Assess this cell for malaria.
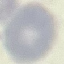

Uninfected.

Summary:
  - Preparation: thin smear
  - Capture: smartphone through the microscope eyepiece
  - Stain: Giemsa
  - Image type: cell patch, automatically extracted from a larger field of view and resized to 64 × 64 pixels